Outline each blood parasite and name the species.
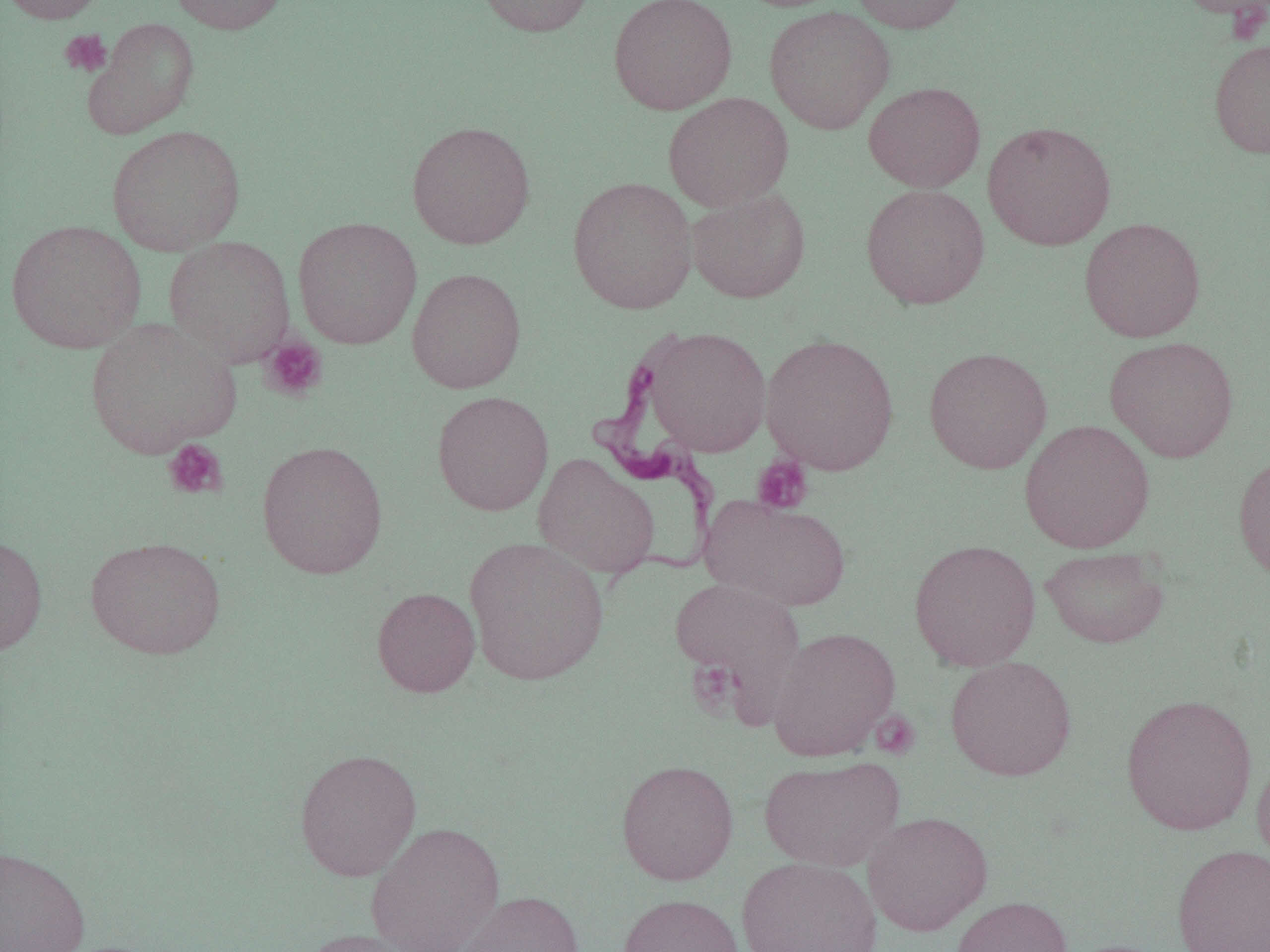

Approximate bounding boxes as (x1, y1, x2, y2) in pixels.
Trypanosoma brucei: (589, 337, 723, 581).
No Plasmodium falciparum, Plasmodium ovale, Plasmodium malariae, Plasmodium vivax, or Babesia divergens observed.

slide-level diagnosis = Trypanosoma brucei
magnification = 1000x
uninfected red blood cell locations = approximate bounding boxes as (x1, y1, x2, y2) in pixels: (0, 0, 112, 24), (167, 0, 289, 35), (474, 0, 596, 37), (608, 0, 738, 114), (849, 0, 969, 34), (1172, 0, 1270, 23), (764, 6, 895, 134), (84, 18, 199, 138), (1209, 38, 1270, 159), (863, 81, 985, 192), (663, 92, 793, 211), (406, 120, 536, 250), (982, 120, 1117, 251), (106, 125, 246, 256), (567, 176, 698, 314), (860, 184, 990, 309), (686, 187, 811, 304), (292, 216, 422, 349), (1079, 217, 1206, 342), (5, 219, 147, 354), (164, 236, 296, 367), (406, 267, 526, 394), (85, 317, 239, 458), (643, 326, 771, 457), (761, 333, 899, 475), (1104, 335, 1239, 463), (923, 346, 1053, 474), (431, 390, 554, 516), (1018, 419, 1155, 554), (256, 439, 388, 580), (1232, 451, 1270, 584), (533, 453, 659, 579), (700, 494, 851, 612), (0, 533, 48, 655), (85, 536, 226, 659), (462, 536, 610, 685), (908, 539, 1041, 671), (1040, 546, 1169, 648), (670, 577, 805, 712), (372, 587, 480, 697), (767, 626, 900, 761), (945, 656, 1077, 781), (1120, 693, 1258, 835), (1252, 746, 1270, 873), (294, 748, 422, 881), (758, 756, 904, 871), (616, 759, 739, 885), (863, 811, 993, 936), (366, 821, 506, 952), (1171, 844, 1270, 952), (0, 845, 91, 952), (736, 856, 881, 952), (451, 890, 584, 952), (618, 893, 744, 952), (951, 895, 1073, 952), (297, 928, 425, 952)
image size = 1270×952 pixels
modality = light microscopy
field of view = one of a larger specimen
platelet locations = approximate bounding boxes as (x1, y1, x2, y2) in pixels: (59, 29, 112, 78), (259, 335, 328, 401), (163, 439, 228, 500), (752, 455, 813, 515), (687, 658, 741, 718)
preparation = thin blood film